Report the malaria status of this cell.
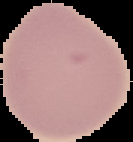
It is uninfected.

From a thin blood smear. Image is 133×142 pixels. Cell region segmented out of the field of view; the surrounding area is masked to black.